Identify the preparation type.
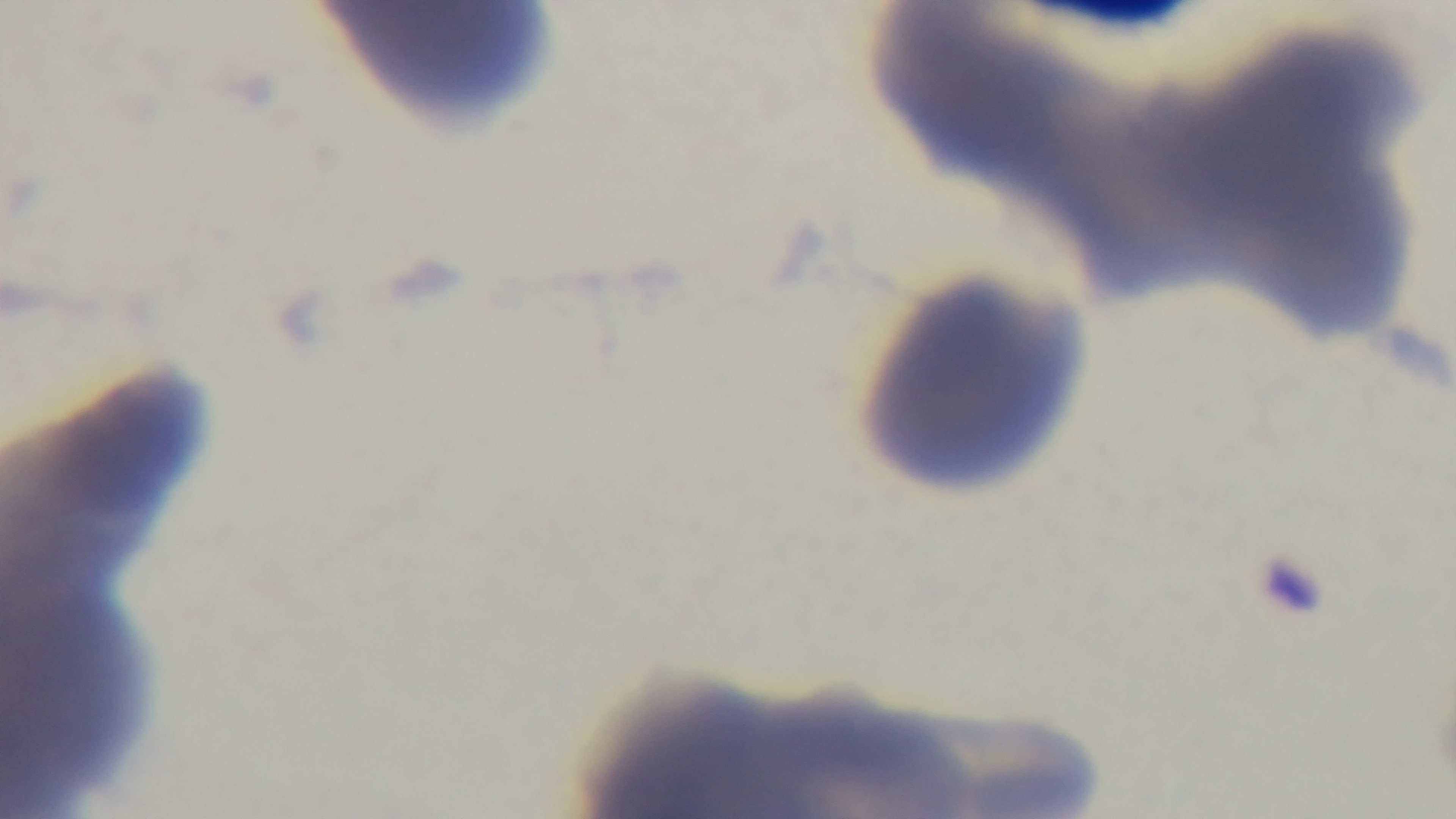
Thin.

Oil-immersion objective, 100x. Photomicrograph. One field from the slide. Giemsa-stained. Malaria status: uninfected. Captured with a mounted 4K digital camera.